Comment on the morphology of the red blood cells.
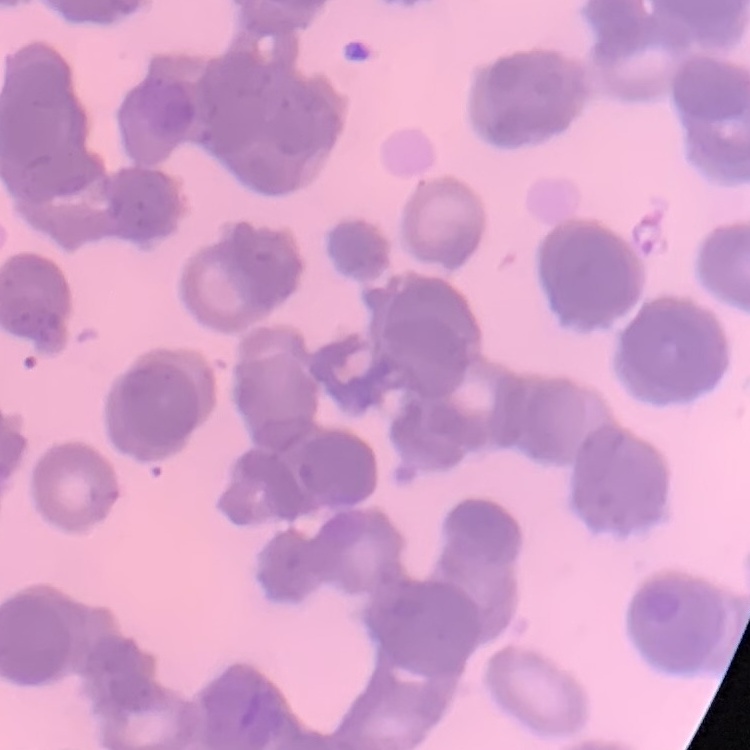
Rouleaux formation.

Summary:
  - Preparation: thin peripheral smear
  - Stain: Field's or Giemsa
  - Image type: square crop of a larger photomicrograph